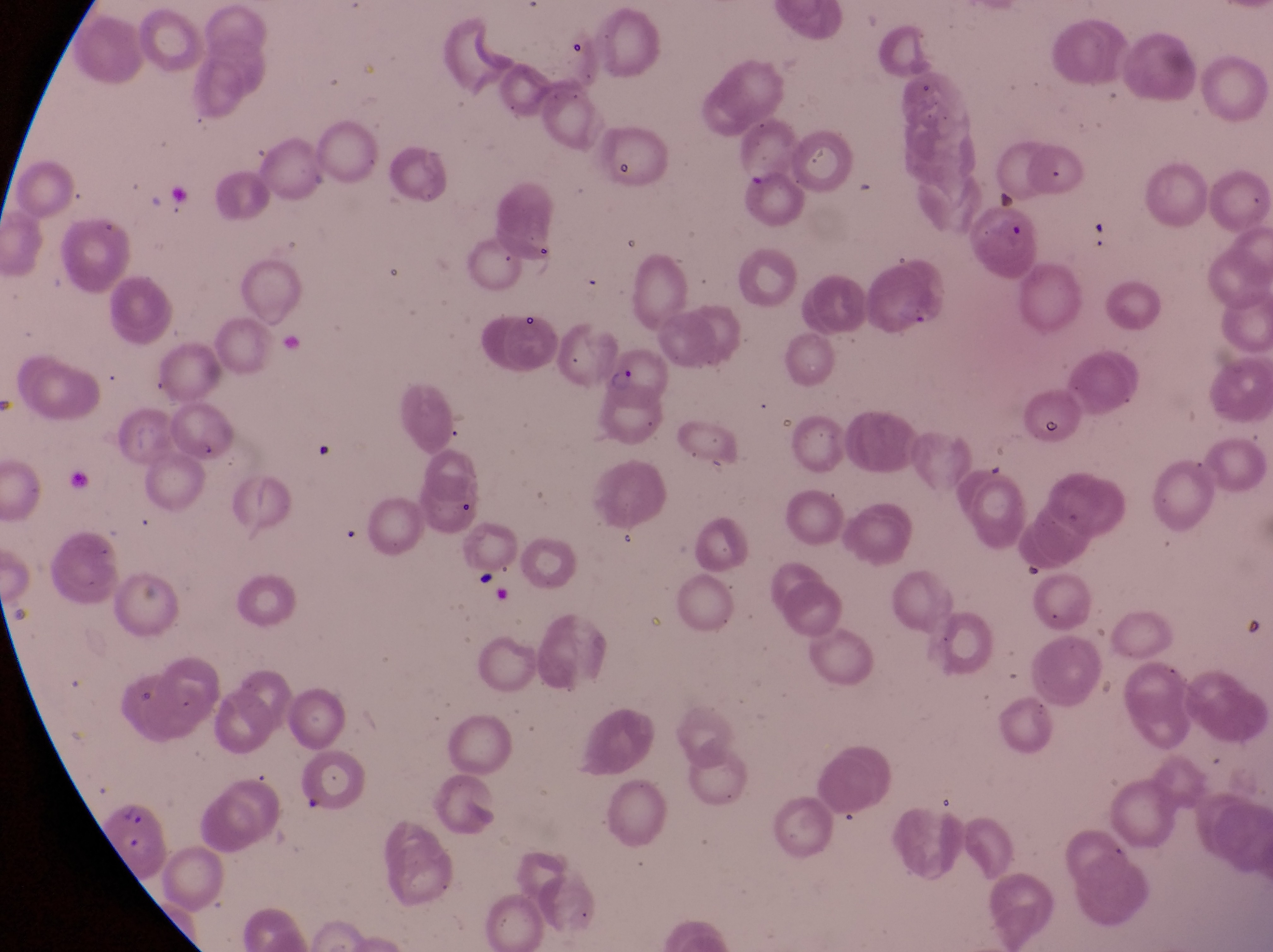 Approximate bounding boxes as [left, top, right, bottom] in pixels. Artifact (platelet-like body, stain precipitate, or debris) locations: [986, 183, 1019, 216]. Parasitised red blood cell locations: [587, 352, 670, 402], [104, 792, 173, 879]. Captured by a smartphone held over the eyepiece of an Olympus CX-23 microscope. Magnification of 1000x. Thin blood smear. Collected in Uganda. Image is 1273×952 pixels. Single field of view.